Outline each blood parasite and name the species.
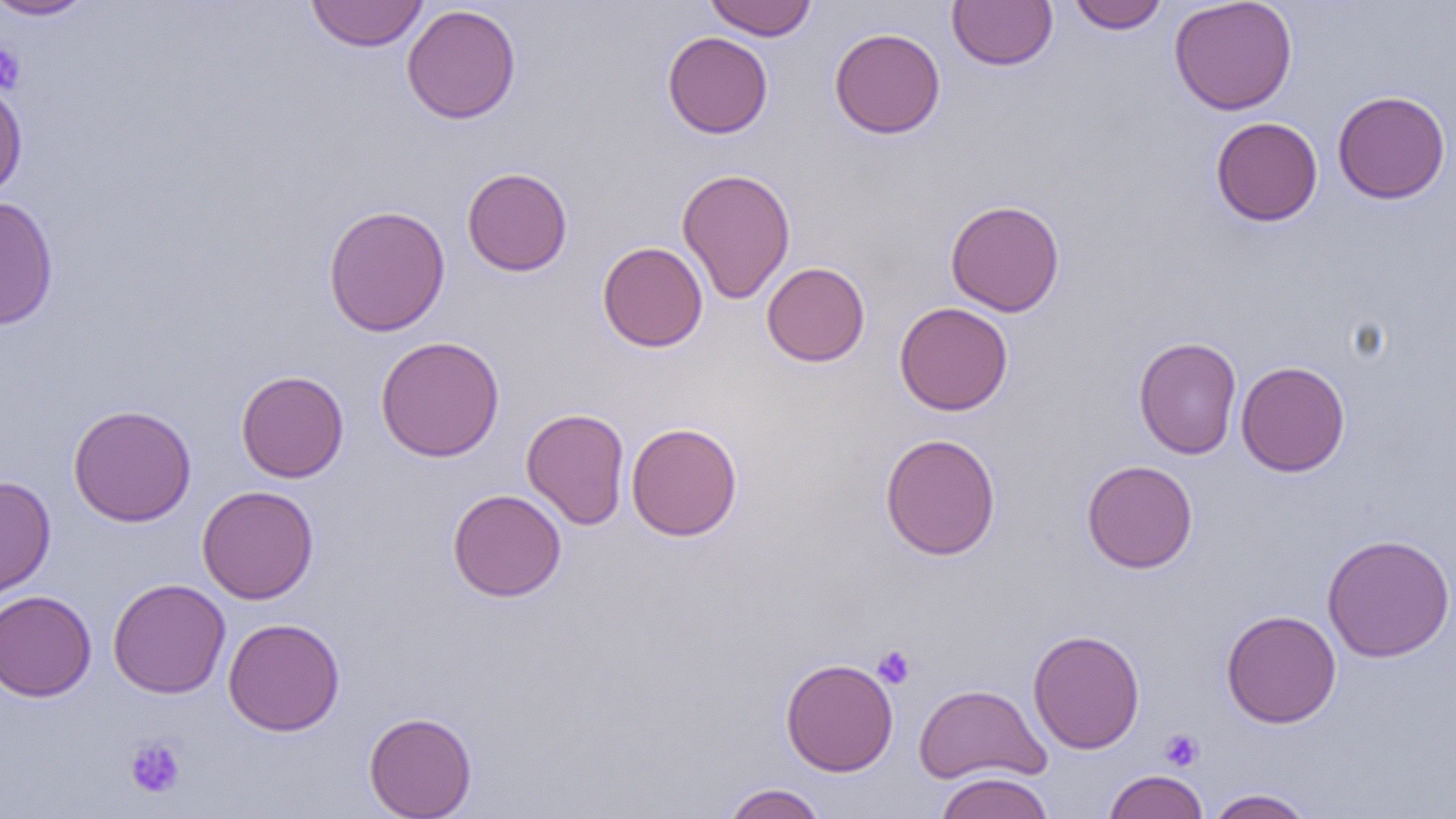
No blood parasites seen.

Approximate bounding boxes as (x1,y1)-(x2,y2) corner pairs in pixels. Platelet locations: (0,43)-(26,94), (873,645)-(915,688), (1160,729)-(1204,771), (124,736)-(186,799). Uninfected red blood cell locations: (0,0)-(97,20), (305,0)-(429,52), (704,0)-(817,41), (947,0)-(1058,70), (1068,0)-(1170,33), (1168,0)-(1298,115), (401,4)-(521,125), (829,27)-(946,139), (662,31)-(773,138), (0,79)-(27,202), (1332,90)-(1451,204), (1210,116)-(1323,226), (462,167)-(573,276), (677,168)-(796,304), (1,195)-(59,330), (945,199)-(1065,316), (323,204)-(451,337), (597,241)-(708,352), (761,262)-(870,366), (894,302)-(1013,416), (375,335)-(505,462), (1133,336)-(1242,460), (1235,360)-(1351,477), (236,370)-(349,483), (68,404)-(197,526), (521,407)-(630,530), (625,422)-(743,541), (880,433)-(1001,560), (1082,460)-(1198,573), (0,476)-(56,600), (196,485)-(319,604), (448,488)-(567,602), (1322,533)-(1455,662), (107,578)-(231,698), (0,590)-(97,702), (1221,609)-(1341,728), (223,617)-(346,735), (1028,629)-(1145,754), (780,658)-(898,777), (913,683)-(1051,785), (364,711)-(478,819), (1102,770)-(1209,819), (932,772)-(1056,819), (721,783)-(829,819), (1204,788)-(1317,818). Slide-level diagnosis: no evidence of blood parasites. Thin blood film. 1000x magnification. Light microscopy. One field of a larger specimen. Image is 1456×819 pixels.